Report the malaria status of this cell.
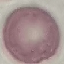
Uninfected.

Summary:
  - Stain: Giemsa
  - Preparation: thin blood smear
  - Capture: smartphone through the microscope eyepiece
  - Image type: automatically extracted cell patch, resized to 64 × 64 pixels